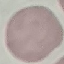 Malaria status: uninfected. Thin blood smear. Giemsa stain. Automatically extracted cell patch, resized to 64 × 64 pixels. Acquired by smartphone through the microscope eyepiece.